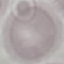
Result: no malaria parasites detected. Thin blood film. Acquired by smartphone through the microscope eyepiece. Automatically extracted cell patch, resized to 64 × 64 pixels. Giemsa stain.